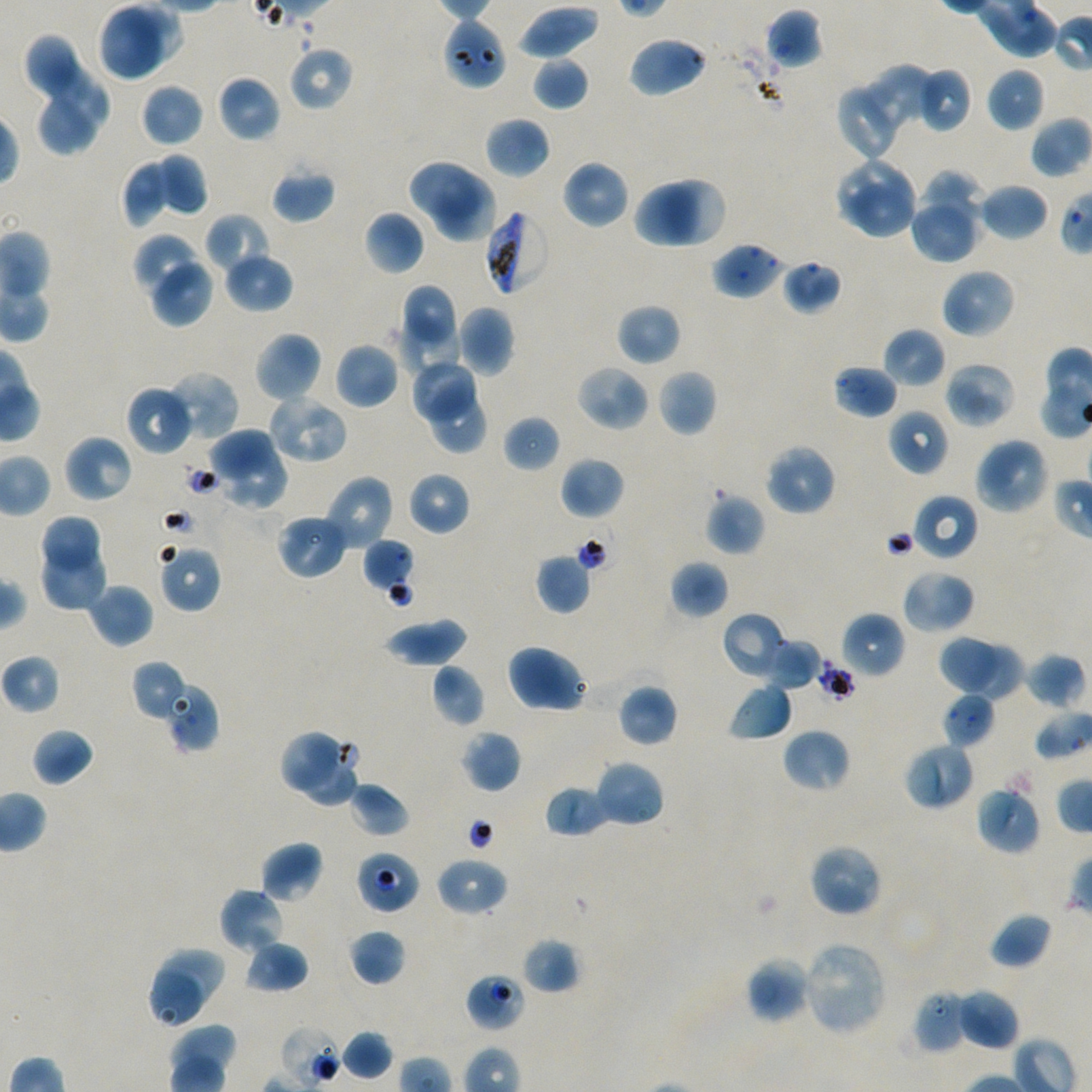

Approximate bounding boxes as {x1, y1, x2, y2} in pixels. Not every red blood cell is marked.
Summary:
  - Locations of uninfected red blood cells: {97, 3, 165, 82}, {517, 5, 600, 60}, {765, 7, 823, 69}, {24, 33, 79, 99}, {627, 35, 708, 98}, {288, 45, 354, 112}, {531, 56, 589, 111}, {43, 60, 110, 134}, {858, 63, 938, 139}, {922, 67, 972, 132}, {986, 67, 1045, 132}, {217, 75, 281, 143}, {141, 82, 204, 147}, {835, 88, 895, 162}, {39, 96, 96, 156}, {484, 115, 551, 179}, {154, 152, 208, 215}, {835, 157, 913, 225}, {407, 158, 480, 220}, {121, 159, 172, 228}, {561, 160, 630, 230}, {272, 168, 336, 224}, {920, 170, 986, 230}, {431, 179, 496, 243}, {667, 179, 726, 247}, {634, 183, 697, 249}, {979, 183, 1049, 241}, {848, 185, 919, 240}, {909, 206, 981, 263}, {364, 211, 424, 275}, {205, 213, 272, 275}, {132, 233, 204, 297}, {223, 252, 293, 313}, {149, 259, 215, 327}, {782, 259, 842, 314}, {941, 268, 1015, 339}, {401, 284, 460, 345}, {616, 303, 682, 366}, {455, 305, 515, 376}, {397, 316, 463, 381}, {883, 327, 946, 388}, {253, 330, 323, 403}, {334, 341, 399, 410}, {409, 359, 480, 427}, {943, 361, 1017, 429}, {575, 365, 651, 432}, {833, 365, 899, 418}, {657, 369, 718, 437}, {162, 370, 240, 443}, {425, 384, 488, 455}, {126, 385, 194, 457}, {265, 391, 350, 465}, {888, 408, 949, 476}, {503, 416, 561, 473}, {211, 426, 274, 477}, {63, 434, 134, 503}, {973, 437, 1050, 515}, {764, 443, 837, 516}, {223, 452, 287, 511}, {560, 456, 625, 520}, {407, 471, 471, 536}, {323, 474, 395, 551}, {706, 492, 765, 556}, {913, 493, 979, 561}, {276, 513, 348, 579}, {43, 515, 101, 569}, {158, 543, 222, 613}, {41, 546, 106, 609}, {535, 553, 592, 615}, {669, 560, 728, 618}, {900, 568, 976, 635}, {88, 583, 153, 648}, {721, 611, 789, 680}, {840, 611, 905, 679}, {382, 617, 468, 668}, {937, 635, 998, 692}, {763, 638, 821, 690}, {963, 640, 1022, 703}, {506, 644, 591, 714}, {1023, 651, 1087, 709}, {131, 660, 189, 721}, {431, 664, 486, 727}, {166, 681, 218, 752}, {617, 682, 678, 747}, {727, 682, 793, 742}, {941, 691, 997, 749}, {31, 727, 94, 786}, {782, 728, 850, 793}, {278, 729, 360, 807}, {462, 730, 522, 793}, {903, 742, 975, 811}, {594, 759, 666, 829}, {348, 780, 410, 837}, {975, 784, 1041, 855}, {544, 785, 611, 838}, {260, 841, 324, 903}, {808, 843, 884, 917}, {436, 856, 508, 917}, {219, 887, 286, 954}, {989, 912, 1053, 969}, {348, 928, 407, 986}, {522, 937, 581, 994}, {244, 939, 309, 993}, {800, 941, 888, 1035}, {158, 945, 224, 1009}, {746, 957, 813, 1023}, {147, 967, 205, 1030}, {955, 988, 1019, 1051}, {340, 1030, 393, 1080}
  - Locations of red blood cells of indeterminate infection status: {442, 17, 507, 91}, {712, 242, 786, 300}, {361, 537, 416, 596}, {816, 659, 855, 704}, {355, 850, 420, 915}, {465, 972, 526, 1032}, {912, 989, 968, 1054}, {279, 1025, 344, 1089}
  - Locations of infected red blood cells: {484, 207, 551, 295}
  - Donor blood group: A+/O+
  - Objective: 100x, oil immersion, numerical aperture 1.45
  - Preparation: thin blood film
  - Culture: static in-vitro Plasmodium falciparum strain NF54
  - Stain: Giemsa
  - Image size: 1092×1092 pixels
  - Field of view: one from this slide